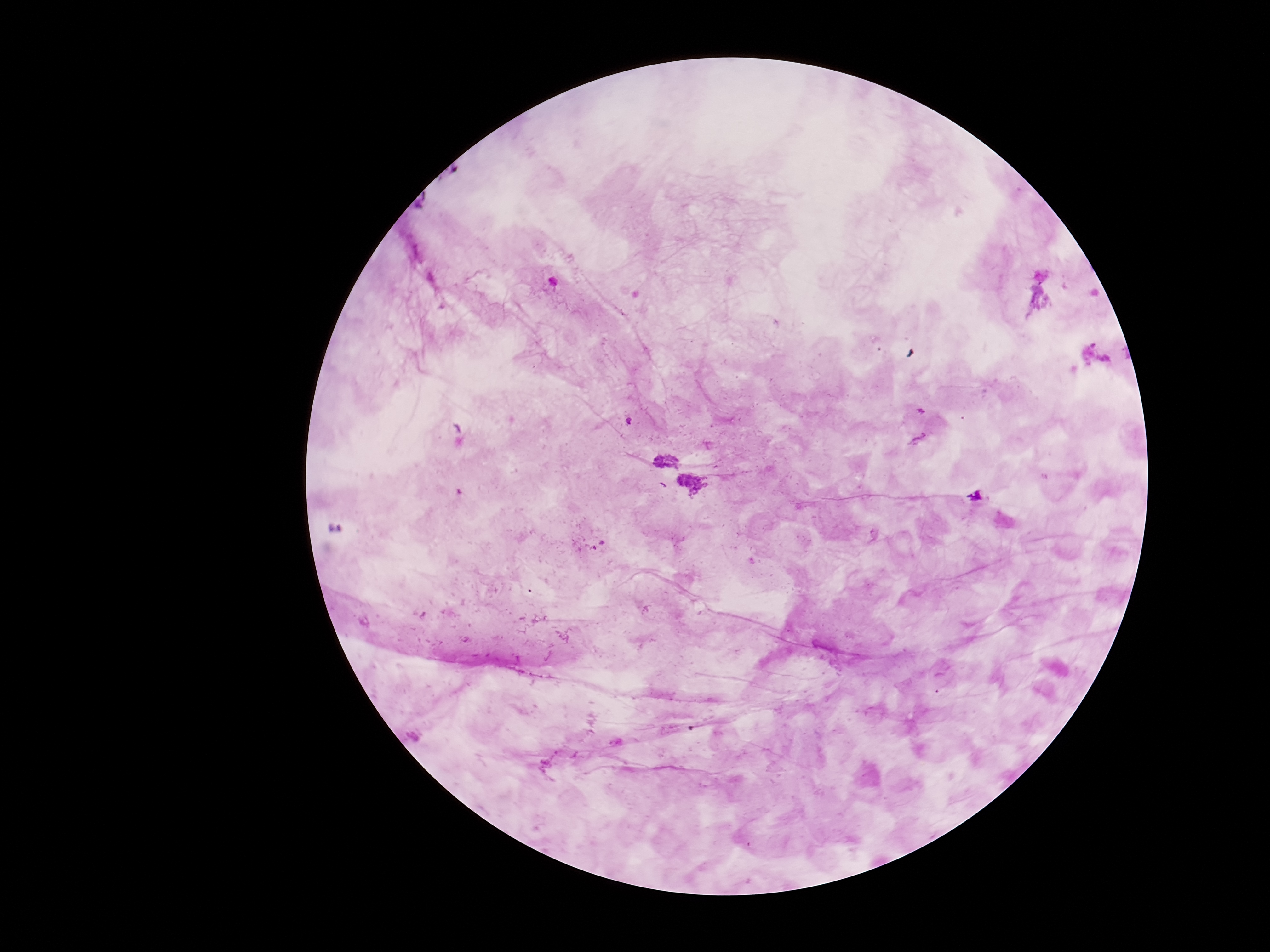

Approximate centers as [x, y] in pixels.
Summary:
  - Plasmodium parasite locations: [664, 459], [693, 485]
  - Patient malaria status: infected
  - Preparation: thick blood smear
  - Stain: Giemsa
  - Magnification: 100x
  - Capture: smartphone camera through the microscope eyepiece
  - Image size: 1270×952 pixels
  - Field of view: single